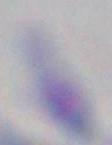

identification = Toxoplasma gondii
modality = micrograph
magnification = 1000x